Locate and identify every blood parasite.
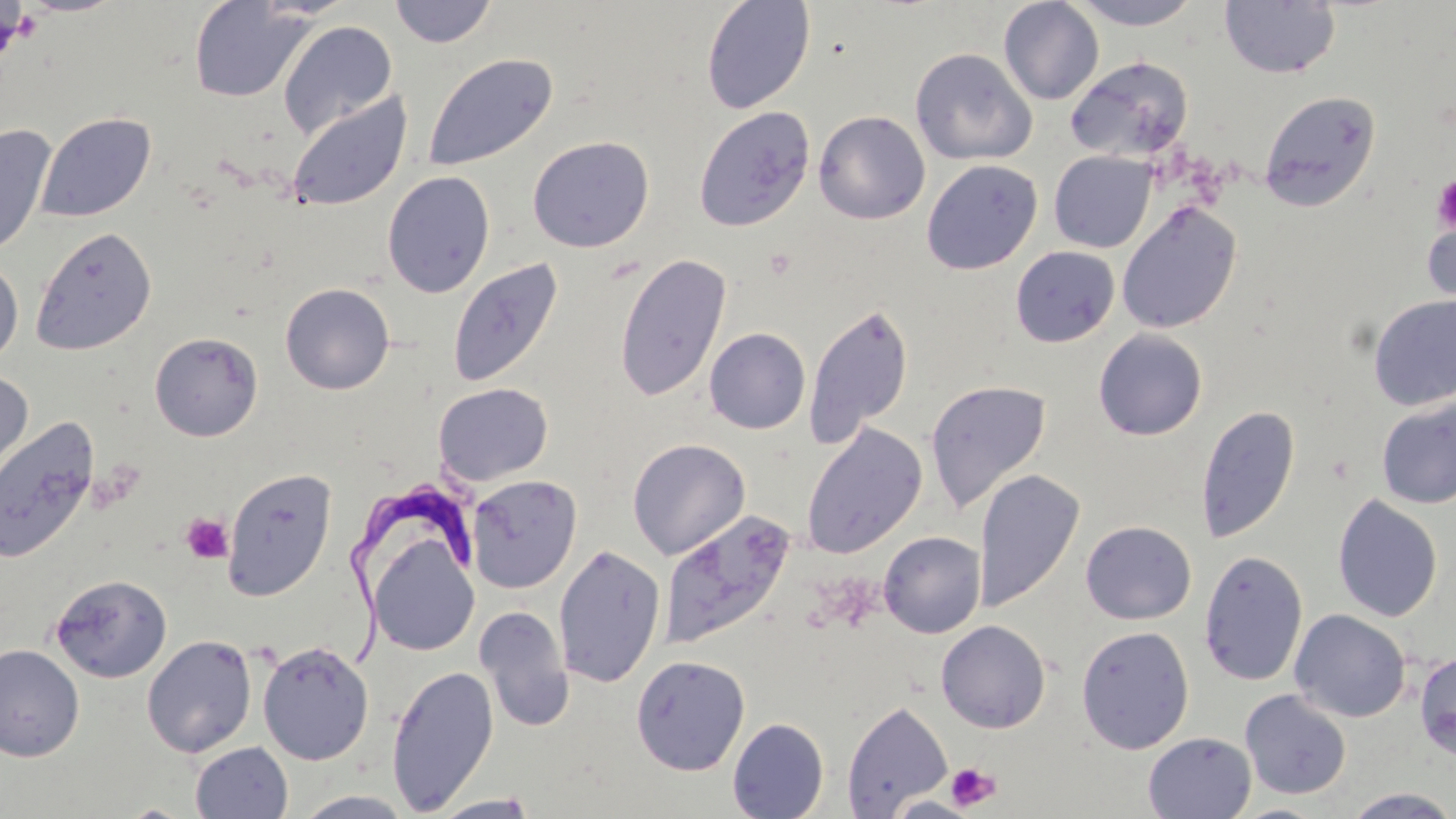

Approximate bounding boxes as [x1, y1, x2, y2] in pixels.
Trypanosoma brucei: [349, 474, 476, 663].
No Plasmodium falciparum, Plasmodium ovale, Plasmodium malariae, Plasmodium vivax, or Babesia divergens observed.

Platelet locations: [0, 3, 33, 65], [1432, 175, 1456, 233], [181, 513, 233, 563], [946, 763, 1001, 811]. Uninfected red blood cell locations: [389, 0, 498, 48], [700, 0, 816, 114], [1071, 0, 1202, 30], [189, 1, 313, 102], [998, 1, 1104, 105], [1220, 1, 1340, 79], [278, 20, 398, 141], [910, 47, 1037, 166], [422, 53, 558, 173], [1065, 56, 1194, 164], [1260, 90, 1382, 212], [286, 91, 412, 212], [694, 107, 815, 232], [813, 110, 930, 225], [34, 112, 156, 224], [0, 123, 57, 260], [527, 135, 654, 253], [1049, 151, 1156, 253], [921, 159, 1043, 275], [381, 170, 495, 298], [1116, 201, 1242, 334], [1421, 205, 1456, 324], [31, 226, 157, 355], [1010, 245, 1120, 348], [614, 252, 732, 403], [0, 258, 23, 366], [448, 258, 563, 388], [280, 283, 395, 394], [1368, 293, 1456, 411], [803, 301, 915, 448], [704, 328, 811, 434], [1094, 329, 1208, 440], [149, 331, 262, 441], [0, 369, 34, 490], [925, 380, 1051, 514], [433, 382, 553, 486], [1376, 397, 1456, 509], [1196, 404, 1300, 543], [0, 418, 100, 564], [801, 423, 927, 559], [628, 439, 750, 559], [222, 468, 337, 601], [973, 469, 1085, 612], [466, 475, 581, 593], [1332, 494, 1443, 622], [659, 509, 795, 649], [1081, 520, 1196, 625], [878, 531, 986, 638], [368, 534, 479, 656], [553, 544, 666, 688], [1198, 550, 1308, 687], [50, 574, 172, 683], [474, 606, 573, 731], [1290, 609, 1411, 722], [936, 620, 1051, 733], [1076, 625, 1195, 754], [141, 634, 258, 758], [257, 642, 374, 765], [0, 644, 85, 762], [1415, 649, 1456, 762], [630, 654, 750, 776], [386, 665, 498, 814], [1240, 689, 1352, 800], [842, 700, 953, 817], [727, 717, 829, 818], [1143, 731, 1257, 818], [190, 741, 293, 819], [1341, 788, 1456, 818], [294, 790, 416, 818], [427, 794, 541, 818], [883, 794, 984, 818], [1228, 803, 1333, 818]. Slide-level diagnosis: Trypanosoma brucei. May-Grünwald-Giemsa-stained preparation. Captured at 1000x magnification. Optical microscopy. Image is 1456×819 pixels. One field of a larger specimen. Thin blood smear.